Identify the blood parasite species.
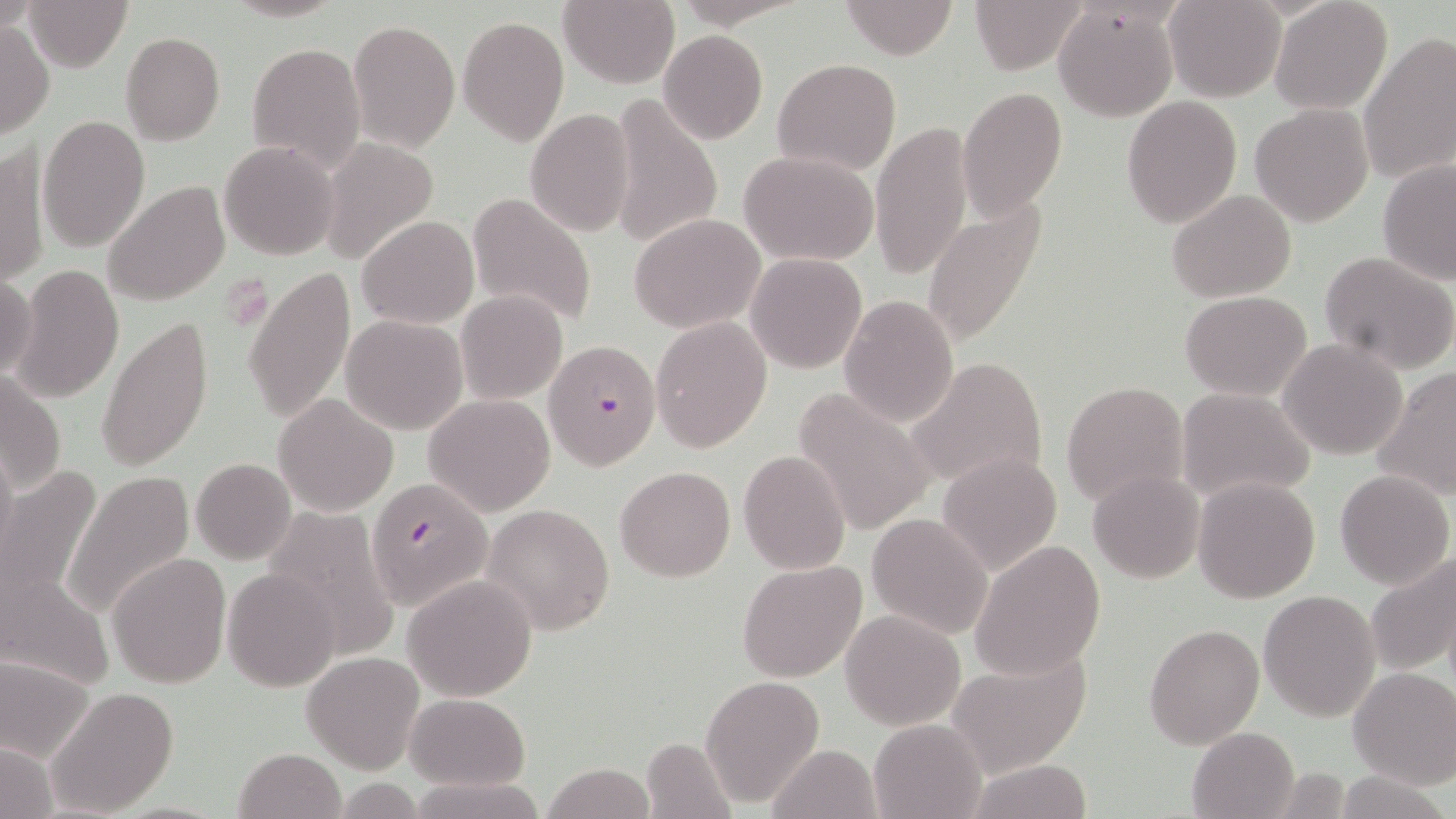
Plasmodium falciparum.

magnification: 1000x
platelet_locations: 'approximate bounding boxes as (x1,y1)-(x2,y2) corner pairs in pixels: (214,275)-(276,318)'
field_of_view: one of a larger specimen
preparation: thin blood smear
uninfected_red_blood_cell_locations: 'approximate bounding boxes as (x1,y1)-(x2,y2) corner pairs in pixels: (22,0)-(134,71), (557,0)-(679,87), (839,0)-(960,59), (970,0)-(1085,75), (1163,0)-(1286,101), (1270,0)-(1393,114), (1053,7)-(1177,120), (458,14)-(569,145), (0,19)-(53,139), (348,19)-(461,153), (659,30)-(766,142), (120,33)-(225,143), (1358,34)-(1455,185), (246,41)-(365,176), (773,57)-(903,176), (957,86)-(1066,220), (608,92)-(725,249), (1121,96)-(1243,228), (1250,103)-(1376,228), (524,108)-(636,238), (39,114)-(151,254), (870,121)-(974,279), (315,138)-(440,264), (218,140)-(339,260), (1,143)-(48,289), (739,150)-(879,264), (1378,159)-(1455,285), (103,180)-(230,306), (1167,190)-(1297,304), (467,191)-(599,329), (922,196)-(1049,348), (629,213)-(767,333), (357,215)-(478,328), (1319,251)-(1456,375), (746,253)-(867,374), (10,264)-(123,404), (244,266)-(355,427), (0,274)-(37,379), (455,290)-(569,405), (1180,291)-(1312,400), (839,294)-(959,428), (95,315)-(214,474), (342,315)-(469,435), (652,316)-(772,452), (1279,338)-(1407,461), (906,355)-(1050,494), (1374,368)-(1456,500), (2,372)-(66,496), (1060,381)-(1189,507), (792,385)-(934,535), (1176,386)-(1318,505), (425,393)-(553,515), (273,394)-(397,515), (0,443)-(16,563), (737,451)-(851,574), (938,451)-(1062,576), (191,456)-(296,564), (0,464)-(103,606), (615,465)-(737,582), (1088,469)-(1205,583), (1335,470)-(1453,588), (65,471)-(195,618), (1193,476)-(1321,604), (483,502)-(616,635), (263,508)-(402,659), (866,513)-(993,640), (970,541)-(1106,680), (108,552)-(233,688), (1364,554)-(1455,674), (737,560)-(867,684), (3,563)-(113,690), (223,567)-(342,692), (402,574)-(538,701), (1258,589)-(1380,722), (841,610)-(964,729), (1144,622)-(1264,750), (945,648)-(1093,777), (300,651)-(425,774), (0,655)-(94,764), (1348,666)-(1456,788), (700,674)-(825,808), (46,687)-(180,816), (404,693)-(531,790), (867,718)-(986,819), (1186,726)-(1301,819), (641,736)-(740,819), (1,742)-(58,818), (769,742)-(883,817), (231,749)-(348,819), (965,759)-(1096,818), (542,760)-(655,819), (1328,772)-(1453,818), (407,775)-(549,819)'
modality: light microscopy
image_size: 1456×819 pixels
plasmodium_falciparum_infected_red_blood_cell_locations: 'approximate bounding boxes as (x1,y1)-(x2,y2) corner pairs in pixels: (541,340)-(661,470), (363,481)-(490,613)'
stain: May-Grünwald-Giemsa